Locate leukocytes (white blood cells).
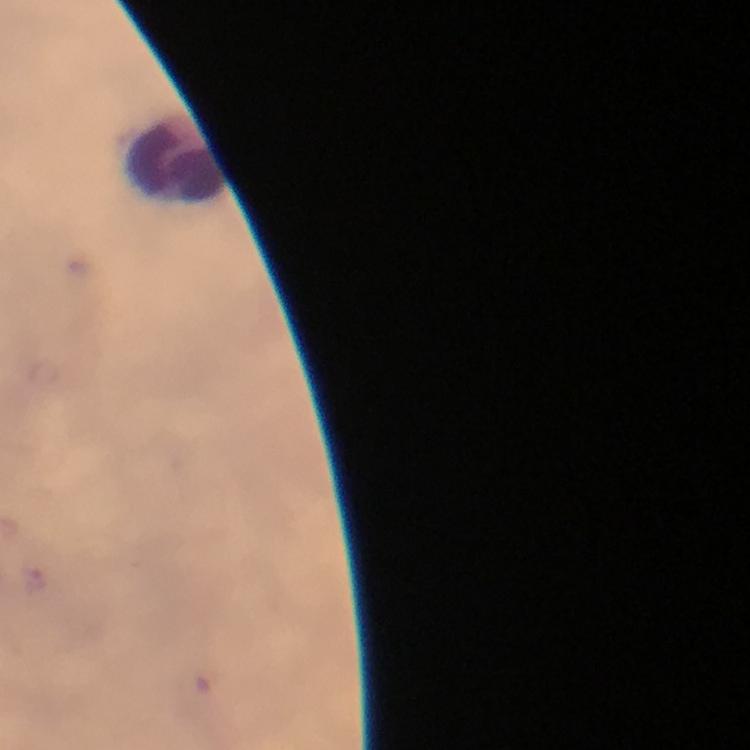
Approximate centers as (x, y) in pixels.
Leukocytes: (179, 161).

stain = Giemsa
immersion oil = applied
capture = smartphone photograph through a microscope
image size = 750×750 pixels
cropped from = one field of view
magnification = 100x
Plasmodium parasites = none detected
preparation = thick blood film
context = from a malaria diagnostic workup